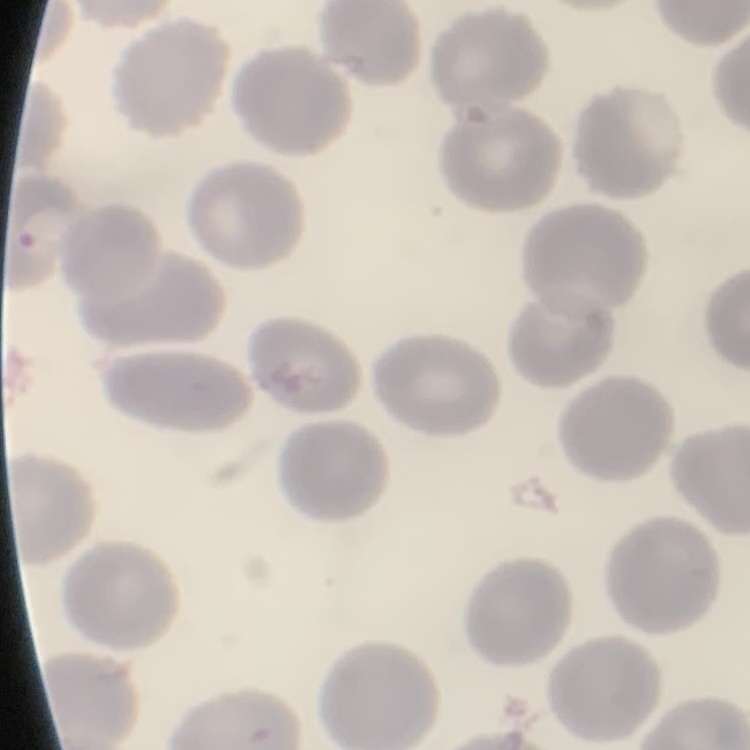 The erythrocytes show no rouleaux formation. One tile cut from a larger photomicrograph. Stained with either Field's or Giemsa. Thin blood film.